Assess this cell for malaria.
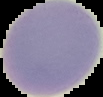
Uninfected.

{
  "image_type": "segmented cell region on a black background",
  "preparation": "thin blood film",
  "image_size": "103×97 pixels"
}